State which parasite is depicted.
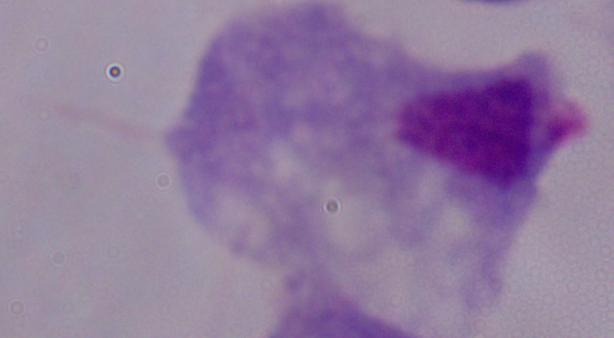
This is a trichomonad.

Photomicrograph. Captured at 1000x magnification.